Name the parasite shown.
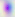
Toxoplasma gondii.

Summary:
  - Magnification: 400x
  - Modality: micrograph